Assess this cell for malaria.
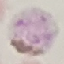

It is parasitized.

Cell patch, automatically extracted from a larger field of view and resized to 64 × 64 pixels. Thin blood smear. Acquired by smartphone through the microscope eyepiece. Giemsa stain.